Look for Plasmodium parasites.
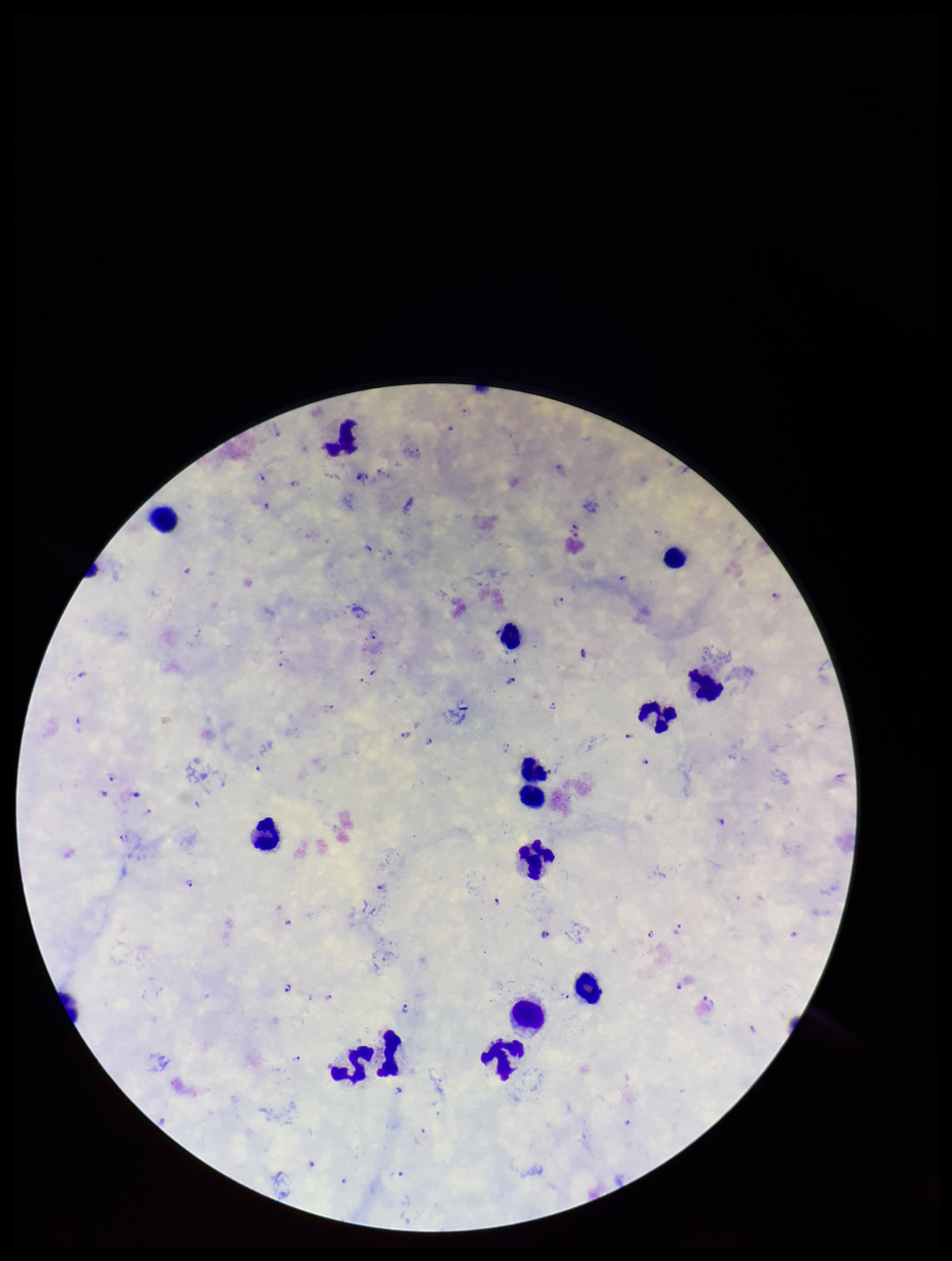
Identified.

image size = 952×1261 pixels
species reported for this patient = Plasmodium falciparum
capture = smartphone photograph through the microscope eyepiece
patient malaria status = infected
parasite count = 39
leukocyte count = 15
preparation = thick blood smear
stain = Giemsa
field of view = one from this slide